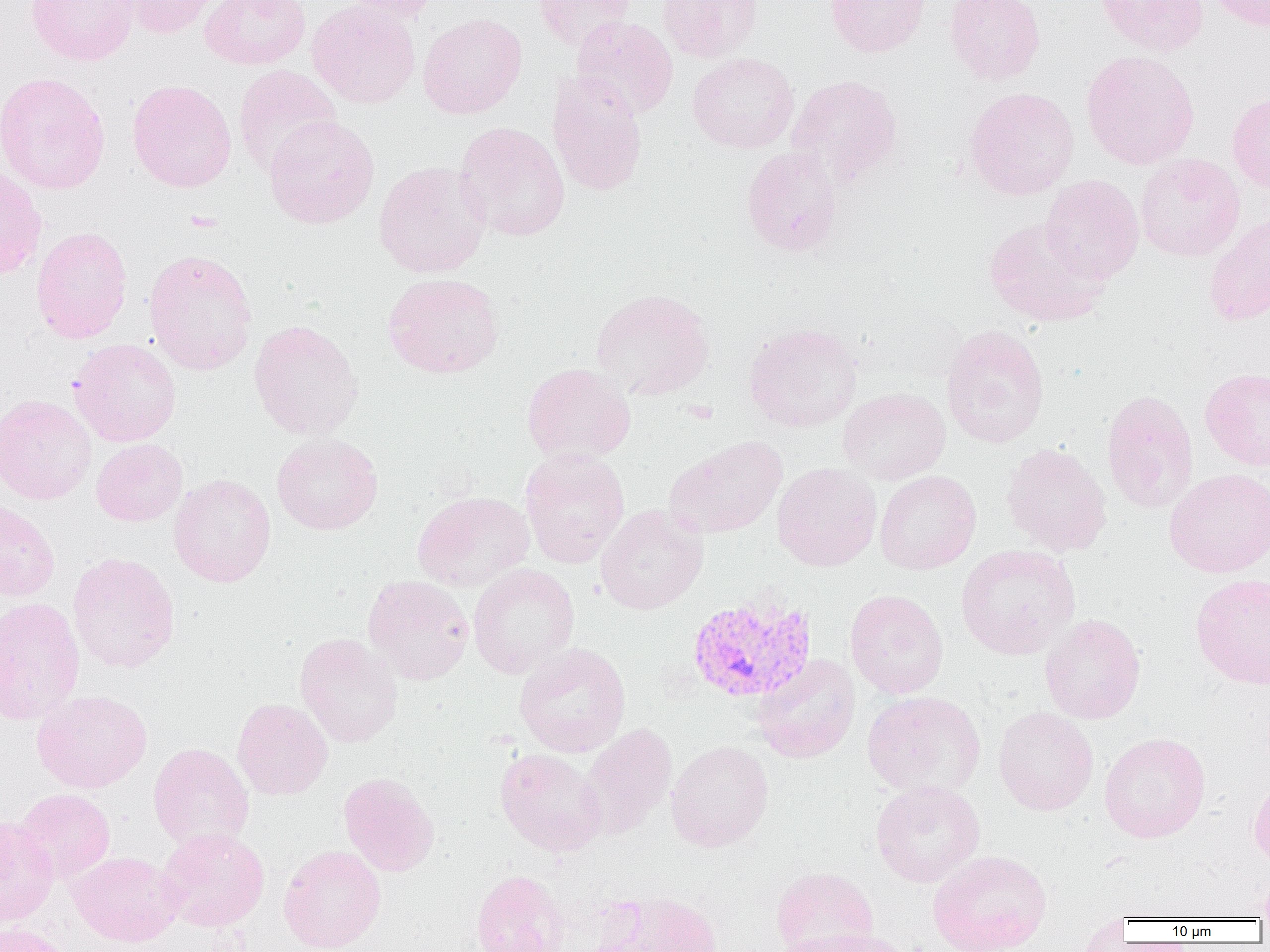
Summary:
  - Coordinate format: approximate bounding boxes as named x1/y1/x2/y2 corners in pixels
  - Plasmodium vivax-infected red blood cell locations: (x1=686, y1=595, x2=816, y2=704)
  - Uninfected red blood cell locations: (x1=26, y1=0, x2=140, y2=65), (x1=119, y1=0, x2=224, y2=39), (x1=199, y1=0, x2=311, y2=70), (x1=338, y1=0, x2=443, y2=22), (x1=531, y1=0, x2=635, y2=51), (x1=657, y1=0, x2=763, y2=62), (x1=825, y1=0, x2=931, y2=57), (x1=945, y1=0, x2=1045, y2=85), (x1=1096, y1=0, x2=1209, y2=56), (x1=1206, y1=0, x2=1270, y2=32), (x1=307, y1=1, x2=421, y2=109), (x1=418, y1=13, x2=527, y2=119), (x1=571, y1=16, x2=678, y2=120), (x1=1081, y1=50, x2=1199, y2=169), (x1=687, y1=52, x2=799, y2=153), (x1=233, y1=65, x2=342, y2=178), (x1=546, y1=71, x2=648, y2=197), (x1=0, y1=72, x2=111, y2=194), (x1=787, y1=74, x2=903, y2=188), (x1=127, y1=79, x2=237, y2=193), (x1=963, y1=86, x2=1079, y2=201), (x1=1227, y1=92, x2=1270, y2=194), (x1=264, y1=115, x2=379, y2=229), (x1=454, y1=122, x2=570, y2=242), (x1=741, y1=146, x2=843, y2=256), (x1=1135, y1=153, x2=1245, y2=262), (x1=373, y1=160, x2=491, y2=278), (x1=0, y1=165, x2=47, y2=280), (x1=1040, y1=175, x2=1144, y2=284), (x1=1204, y1=211, x2=1270, y2=327), (x1=983, y1=217, x2=1110, y2=327), (x1=31, y1=226, x2=133, y2=343), (x1=144, y1=248, x2=258, y2=376), (x1=382, y1=272, x2=504, y2=379), (x1=590, y1=288, x2=715, y2=400), (x1=248, y1=320, x2=363, y2=441), (x1=743, y1=322, x2=862, y2=432), (x1=940, y1=324, x2=1050, y2=449), (x1=69, y1=338, x2=181, y2=446), (x1=522, y1=363, x2=636, y2=464), (x1=1200, y1=367, x2=1270, y2=471), (x1=838, y1=388, x2=950, y2=484), (x1=1100, y1=389, x2=1200, y2=514), (x1=0, y1=394, x2=97, y2=504), (x1=271, y1=433, x2=383, y2=535), (x1=663, y1=436, x2=788, y2=539), (x1=91, y1=438, x2=188, y2=526), (x1=1001, y1=442, x2=1112, y2=556), (x1=519, y1=448, x2=630, y2=568), (x1=772, y1=462, x2=882, y2=571), (x1=1164, y1=468, x2=1270, y2=578), (x1=874, y1=470, x2=981, y2=574), (x1=169, y1=474, x2=276, y2=587), (x1=412, y1=491, x2=535, y2=591), (x1=0, y1=498, x2=60, y2=601), (x1=595, y1=504, x2=708, y2=614), (x1=955, y1=543, x2=1081, y2=660), (x1=67, y1=552, x2=180, y2=673), (x1=468, y1=563, x2=580, y2=678), (x1=1190, y1=573, x2=1270, y2=689), (x1=363, y1=574, x2=475, y2=685), (x1=845, y1=589, x2=949, y2=699), (x1=0, y1=598, x2=85, y2=724), (x1=1039, y1=613, x2=1146, y2=724), (x1=295, y1=633, x2=403, y2=747), (x1=514, y1=642, x2=631, y2=758), (x1=753, y1=654, x2=860, y2=764), (x1=32, y1=689, x2=152, y2=793), (x1=861, y1=690, x2=987, y2=799), (x1=232, y1=697, x2=333, y2=800), (x1=993, y1=707, x2=1099, y2=816), (x1=579, y1=722, x2=678, y2=839), (x1=1099, y1=732, x2=1211, y2=843), (x1=666, y1=739, x2=775, y2=852), (x1=148, y1=742, x2=255, y2=852), (x1=495, y1=748, x2=607, y2=857), (x1=338, y1=772, x2=439, y2=877), (x1=1248, y1=772, x2=1270, y2=871), (x1=871, y1=781, x2=985, y2=887), (x1=16, y1=788, x2=115, y2=882), (x1=0, y1=815, x2=59, y2=925), (x1=157, y1=827, x2=269, y2=932), (x1=279, y1=844, x2=386, y2=952), (x1=928, y1=849, x2=1052, y2=952), (x1=68, y1=851, x2=184, y2=947), (x1=770, y1=866, x2=879, y2=951), (x1=1257, y1=868, x2=1270, y2=919), (x1=470, y1=869, x2=569, y2=952), (x1=601, y1=891, x2=723, y2=952), (x1=0, y1=922, x2=73, y2=952), (x1=783, y1=928, x2=913, y2=952)
  - Slide-level diagnosis: Plasmodium vivax
  - Field of view: single
  - Modality: light microscopy
  - Preparation: thin blood film
  - Magnification: 1000x
  - Image size: 1270×952 pixels